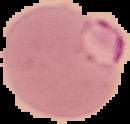

Summary:
  - Image size: 130×124 pixels
  - Image type: segmented cell region on a black background
  - Result: malaria parasites identified
  - Preparation: thin blood smear